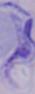

identification = trypanosome
magnification = 1000x
modality = photomicrograph